Name the cell type shown.
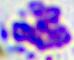
This is a leukocyte.

Captured at 400x magnification. Micrograph.